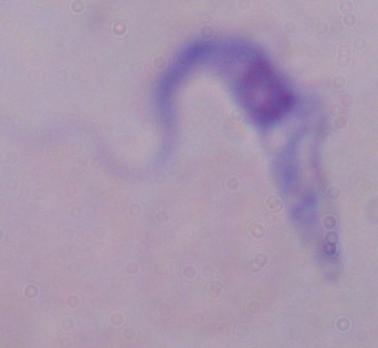

identification = trypanosome
magnification = 1000x
modality = micrograph